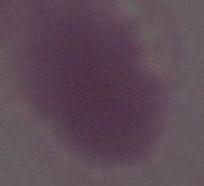

identification = erythrocyte
modality = photomicrograph
magnification = 1000x